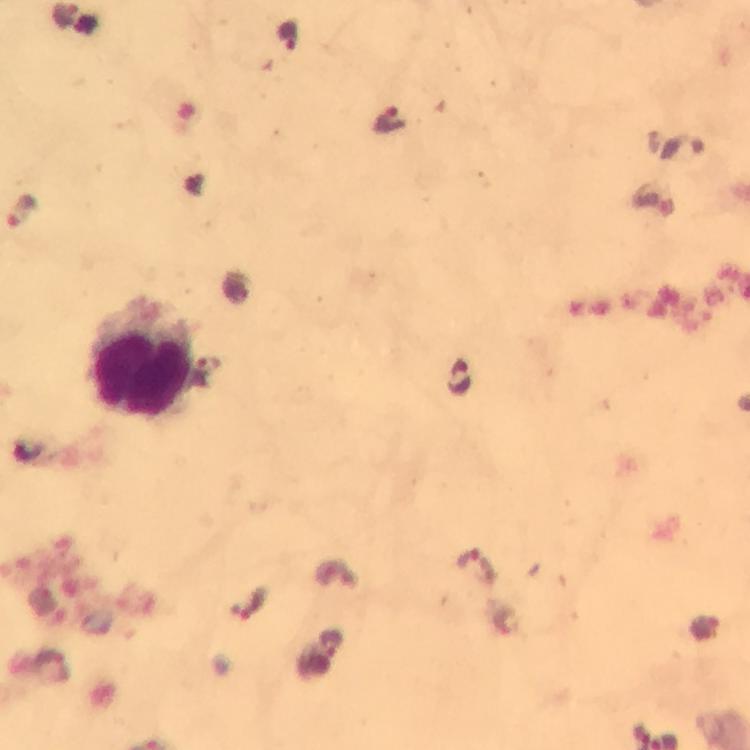

Approximate centers as [x, y] in pixels.
Summary:
  - Plasmodium parasite locations: [392, 121], [684, 147], [458, 377], [477, 568], [248, 604]
  - Leukocyte locations: [140, 358]
  - Immersion oil: used
  - Context: from a diagnostic examination for malaria
  - Magnification: 100x
  - Stain: Giemsa
  - Cropped from: one field of view
  - Preparation: thick blood film
  - Capture: smartphone camera through the microscope
  - Image size: 750×750 pixels